Assess the morphology of the erythrocytes.
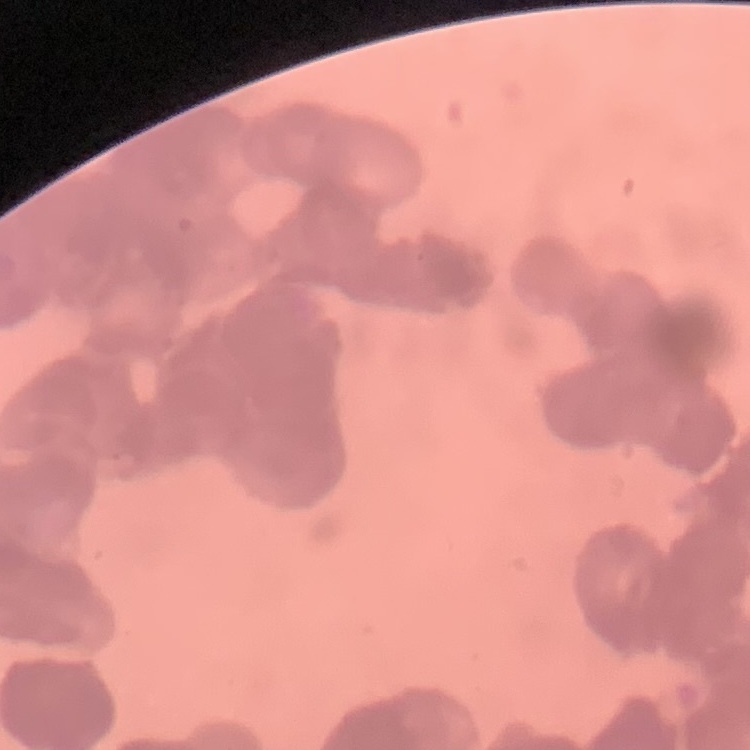
Rouleaux formation.

preparation: thin blood smear
stain: Field's or Giemsa
image_type: one tile cut from a larger photomicrograph